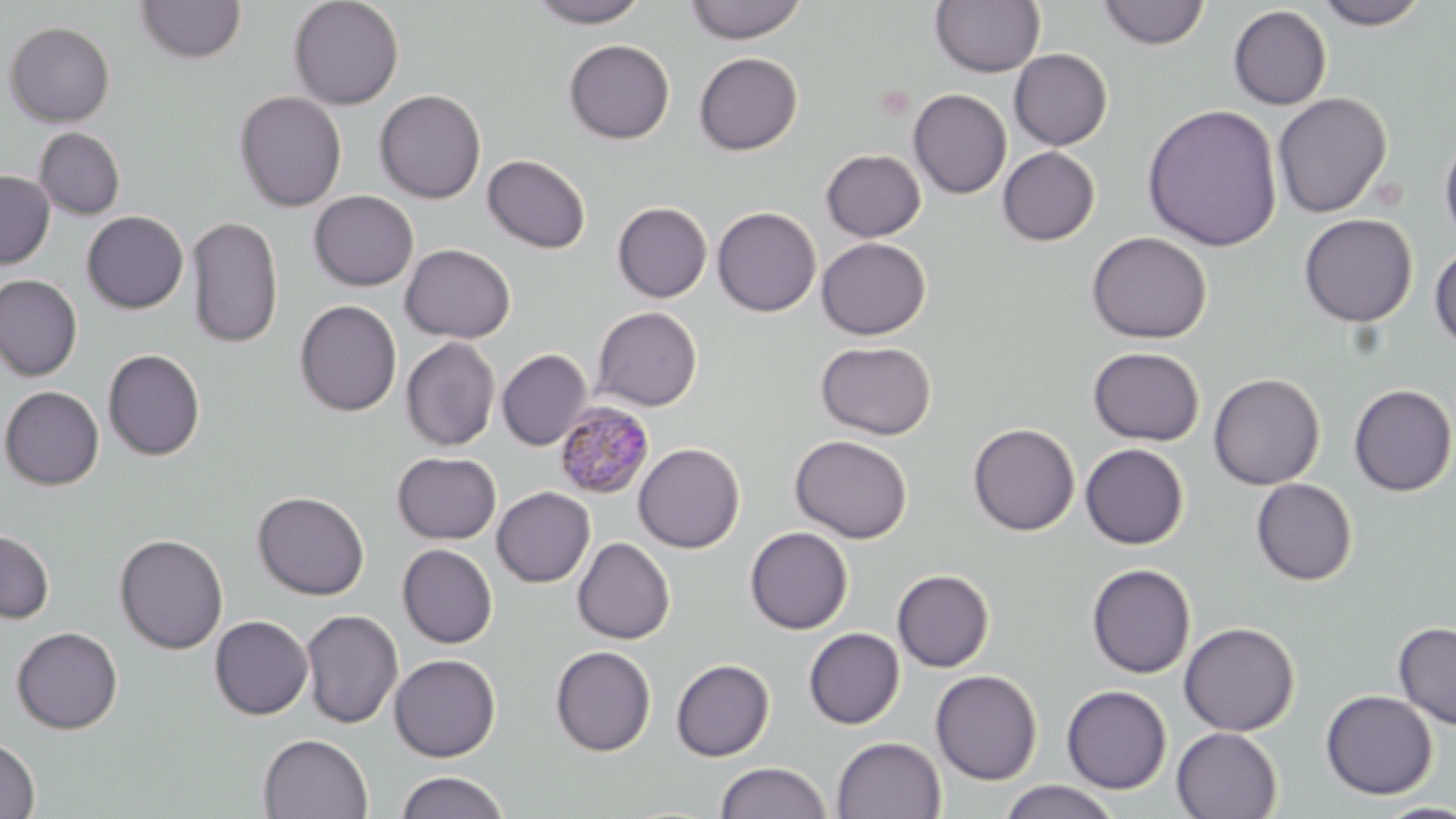

Summary:
  - Coordinate format: approximate bounding boxes as (x1,y1)-(x2,y2) corner pairs in pixels
  - Uninfected red blood cell locations: (287,0)-(405,110), (527,0)-(649,27), (684,0)-(806,43), (930,0)-(1046,77), (1312,0)-(1430,29), (135,1)-(247,64), (1097,1)-(1210,49), (1228,5)-(1332,110), (3,21)-(115,127), (563,39)-(674,144), (1009,48)-(1113,150), (694,51)-(803,155), (908,88)-(1012,198), (374,89)-(486,203), (234,90)-(347,212), (1272,92)-(1392,218), (1142,103)-(1282,252), (34,127)-(126,220), (1439,128)-(1456,251), (997,146)-(1100,245), (821,149)-(925,241), (483,154)-(591,254), (0,170)-(54,268), (309,190)-(418,291), (612,202)-(712,302), (712,206)-(822,316), (82,211)-(188,313), (1299,214)-(1418,327), (186,215)-(284,349), (1086,231)-(1212,343), (816,237)-(930,339), (400,243)-(516,343), (1430,246)-(1456,353), (0,274)-(83,382), (294,299)-(402,416), (592,306)-(702,411), (400,337)-(500,451), (816,340)-(937,440), (1088,346)-(1204,446), (497,348)-(593,451), (103,349)-(205,461), (1208,372)-(1325,489), (1349,383)-(1456,497), (0,386)-(104,490), (968,423)-(1080,536), (790,434)-(912,543), (633,442)-(745,552), (1079,443)-(1189,549), (393,451)-(501,544), (1251,478)-(1358,586), (492,486)-(595,587), (252,490)-(369,600), (0,527)-(55,624), (745,527)-(853,634), (113,533)-(228,654), (572,537)-(675,644), (397,544)-(497,648), (1086,563)-(1196,678), (892,569)-(995,672), (300,609)-(403,728), (209,615)-(313,720), (1179,621)-(1300,736), (1394,621)-(1456,731), (11,626)-(123,733), (803,627)-(905,729), (550,645)-(655,756), (389,654)-(501,762), (671,659)-(775,761), (930,669)-(1042,784), (1062,685)-(1171,793), (1320,690)-(1438,799), (1171,727)-(1283,819), (258,733)-(373,818), (831,736)-(946,818), (0,737)-(40,818), (716,761)-(831,818), (396,771)-(509,819), (998,780)-(1121,818), (1372,801)-(1456,819)
  - Plasmodium malariae-infected red blood cell locations: (554,400)-(655,499)
  - Slide-level diagnosis: Plasmodium malariae
  - Modality: light microscopy
  - Magnification: 1000x
  - Image size: 1456×819 pixels
  - Stain: May-Grünwald-Giemsa
  - Preparation: thin blood film
  - Field of view: one of a larger specimen